Report the malaria status of this cell.
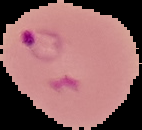

It is parasitized.

image type = cell region segmented out of the field of view; surrounding area masked to black
image size = 142×130 pixels
preparation = thin blood film